Assess this cell for malaria.
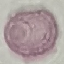

It is uninfected.

Summary:
  - Preparation: thin blood film
  - Capture: smartphone camera at the microscope eyepiece
  - Image type: cell patch, automatically extracted from a larger field of view and resized to 64 × 64 pixels
  - Stain: Giemsa